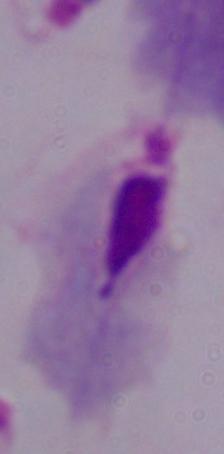

Summary:
  - Identification: trichomonad
  - Magnification: 1000x
  - Modality: photomicrograph